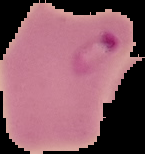 Image is 145×154 pixels. From a thin blood smear. Cell region segmented out of the field of view; the surrounding area is masked to black. Malaria status: parasitized.